Report the malaria status of this cell.
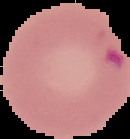

Parasitized.

preparation = thin blood film
image type = cell region segmented out of the field of view; surrounding area masked to black
image size = 130×139 pixels